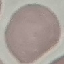
Result: no malaria parasites seen. Thin blood smear. Giemsa-stained preparation. Cell patch, automatically extracted from a larger field of view and resized to 64 × 64 pixels. Photographed with a smartphone camera at the microscope eyepiece.